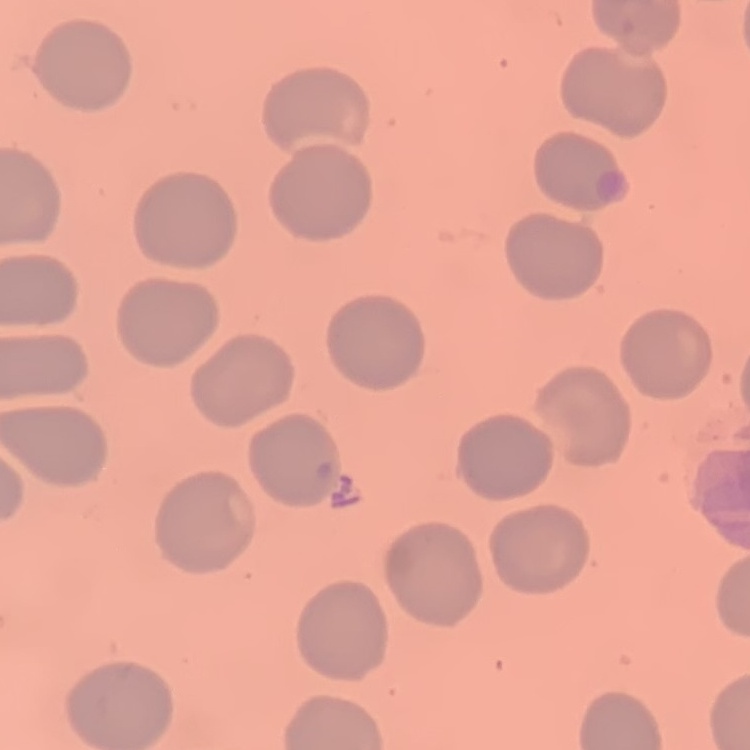
red_blood_cell_morphology: no rouleaux formation
stain: Field's or Giemsa
preparation: thin blood film
image_type: square crop of a larger photomicrograph